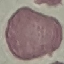

Result: negative for malaria parasites. Acquired by smartphone through the microscope eyepiece. Cell patch, automatically extracted from a larger field of view and resized to 64 × 64 pixels. Giemsa-stained preparation. Thin blood film.